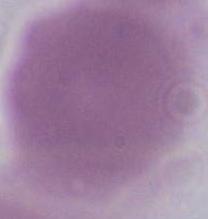

Summary:
  - Modality: micrograph
  - Magnification: 1000x
  - Identification: red blood cell